Assess the morphology of the red blood cells.
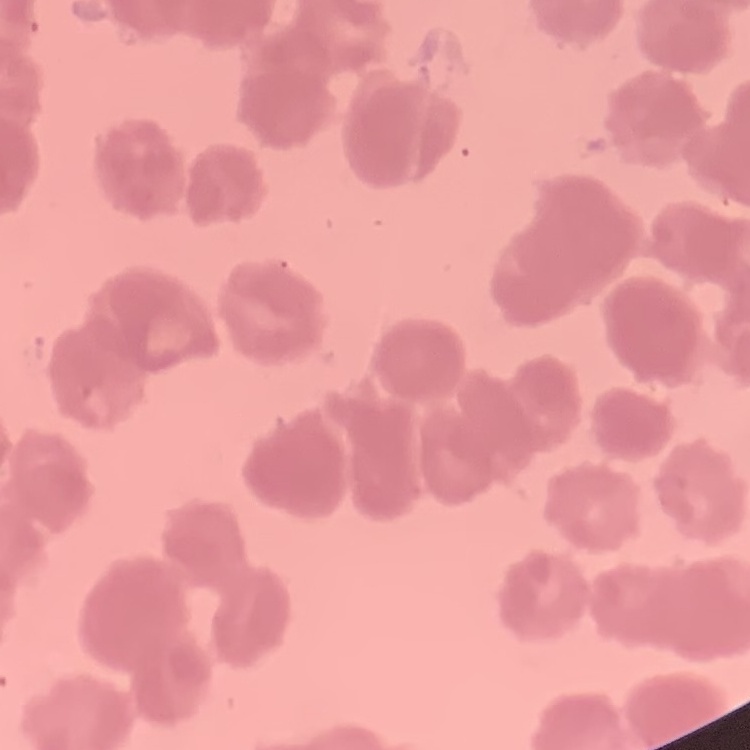
Rouleaux formation.

One tile cut from a larger photomicrograph. Field's or Giemsa stain. Thin peripheral smear.